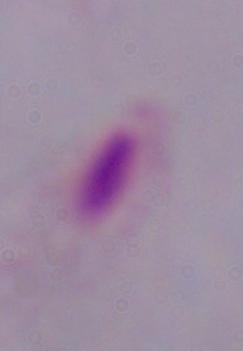

Summary:
  - Magnification: 1000x
  - Modality: photomicrograph
  - Identification: trichomonad